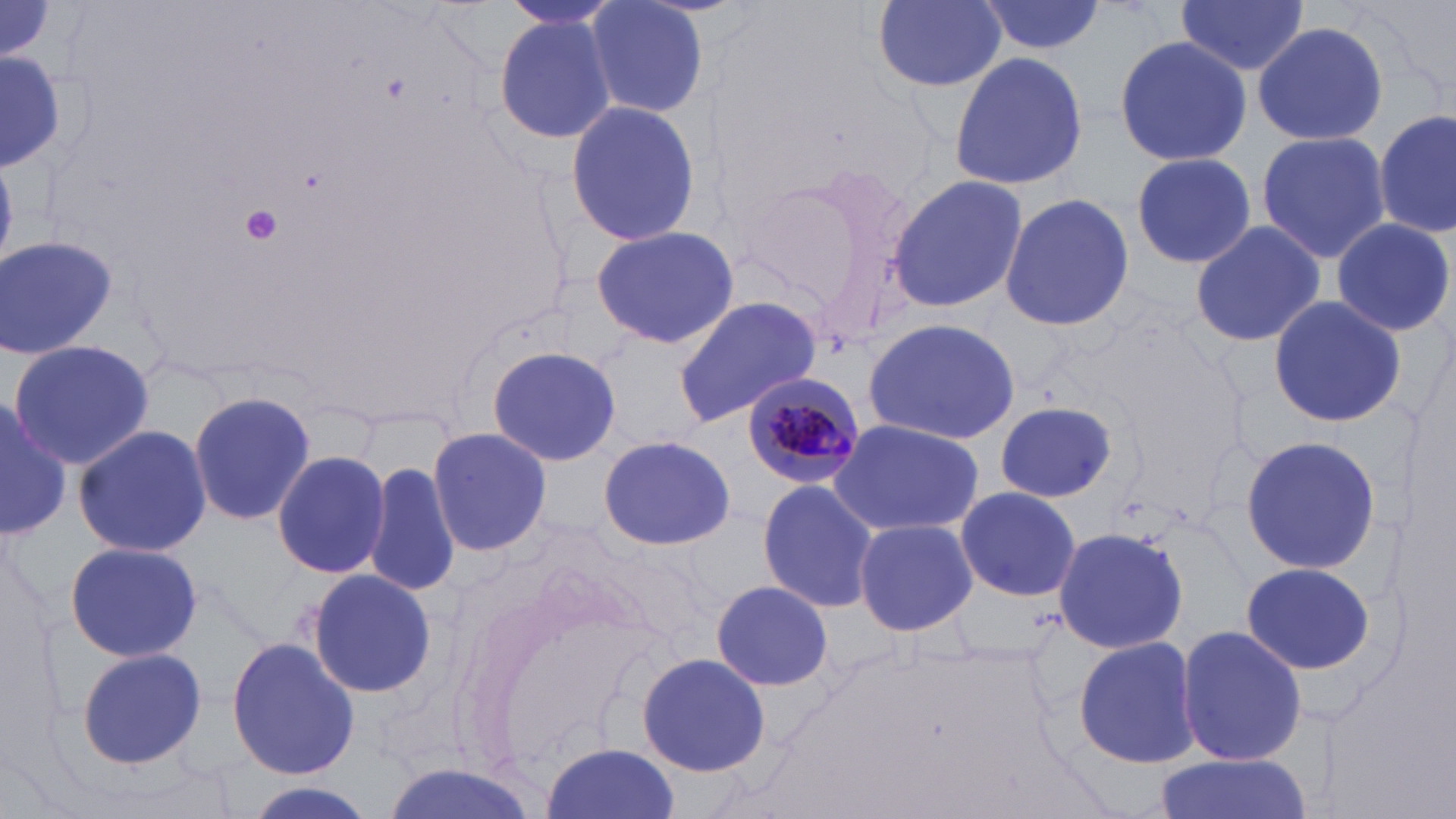

Summary:
  - Coordinate format: approximate bounding boxes as named x1/y1/x2/y2 corners in pixels
  - Uninfected red blood cell locations: (x1=869, y1=0, x2=1011, y2=93), (x1=975, y1=0, x2=1105, y2=58), (x1=1174, y1=0, x2=1311, y2=77), (x1=581, y1=1, x2=709, y2=119), (x1=492, y1=13, x2=618, y2=143), (x1=1252, y1=21, x2=1388, y2=147), (x1=1115, y1=31, x2=1252, y2=168), (x1=0, y1=49, x2=63, y2=170), (x1=950, y1=51, x2=1091, y2=191), (x1=563, y1=100, x2=702, y2=246), (x1=1376, y1=109, x2=1453, y2=241), (x1=1255, y1=130, x2=1391, y2=262), (x1=1128, y1=152, x2=1259, y2=268), (x1=730, y1=158, x2=917, y2=334), (x1=883, y1=173, x2=1029, y2=314), (x1=998, y1=193, x2=1136, y2=330), (x1=1331, y1=217, x2=1456, y2=338), (x1=1189, y1=221, x2=1324, y2=349), (x1=588, y1=224, x2=739, y2=350), (x1=1, y1=234, x2=118, y2=359), (x1=1267, y1=295, x2=1408, y2=430), (x1=673, y1=297, x2=822, y2=428), (x1=861, y1=317, x2=1022, y2=445), (x1=6, y1=339, x2=154, y2=468), (x1=487, y1=344, x2=622, y2=466), (x1=187, y1=388, x2=319, y2=526), (x1=0, y1=395, x2=71, y2=540), (x1=993, y1=402, x2=1117, y2=504), (x1=825, y1=417, x2=985, y2=538), (x1=73, y1=423, x2=212, y2=558), (x1=426, y1=423, x2=553, y2=557), (x1=599, y1=434, x2=738, y2=550), (x1=1239, y1=434, x2=1383, y2=578), (x1=271, y1=450, x2=392, y2=579), (x1=365, y1=461, x2=461, y2=597), (x1=755, y1=478, x2=881, y2=614), (x1=955, y1=484, x2=1082, y2=603), (x1=852, y1=517, x2=979, y2=638), (x1=1052, y1=526, x2=1189, y2=654), (x1=63, y1=539, x2=202, y2=664), (x1=1241, y1=560, x2=1377, y2=676), (x1=306, y1=568, x2=439, y2=699), (x1=708, y1=579, x2=836, y2=693), (x1=1175, y1=626, x2=1310, y2=766), (x1=1073, y1=635, x2=1201, y2=769), (x1=226, y1=636, x2=362, y2=779), (x1=75, y1=646, x2=209, y2=770), (x1=636, y1=650, x2=773, y2=777), (x1=540, y1=742, x2=681, y2=819), (x1=1151, y1=755, x2=1315, y2=819), (x1=233, y1=782, x2=381, y2=819)
  - Platelet locations: (x1=241, y1=204, x2=283, y2=245)
  - Plasmodium malariae-infected red blood cell locations: (x1=739, y1=371, x2=867, y2=492)
  - Slide-level diagnosis: Plasmodium malariae
  - Modality: light microscopy
  - Magnification: 1000x
  - Field of view: single
  - Image size: 1456×819 pixels
  - Stain: May-Grünwald-Giemsa
  - Preparation: thin blood smear